Comment on the morphology of the erythrocytes.
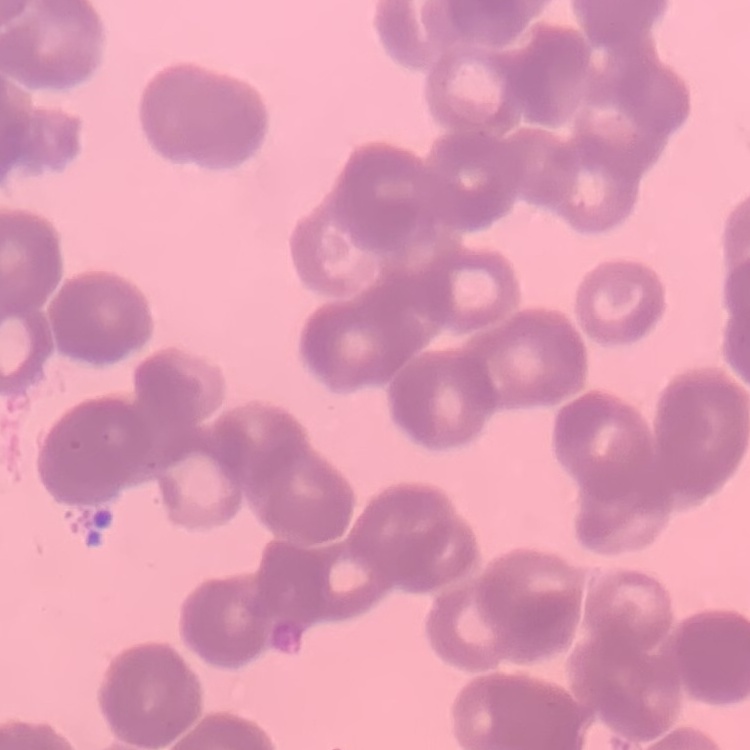
They show rouleaux formation.

stain = Field's or Giemsa
image type = square crop of a larger photomicrograph
preparation = thin blood smear